Point out each Plasmodium parasite.
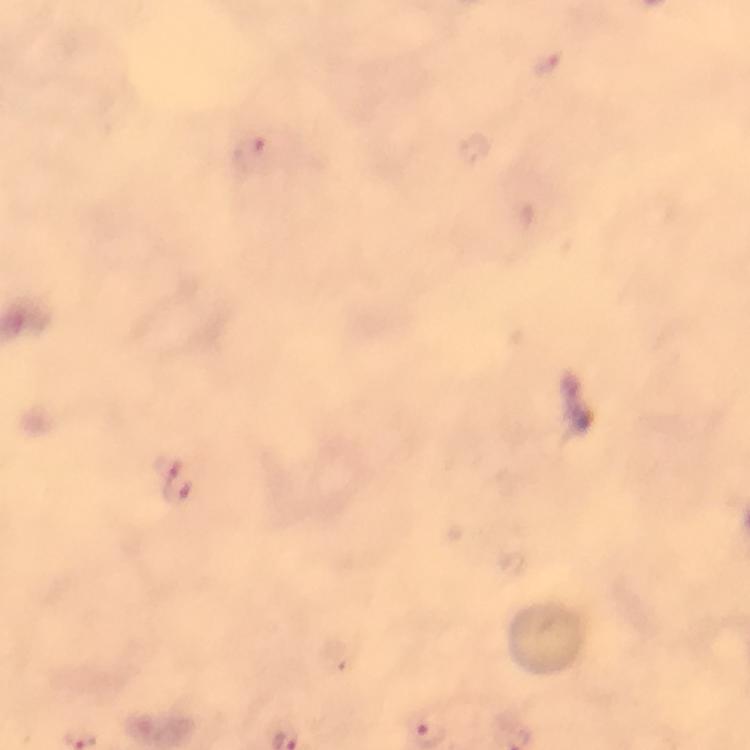
Approximate centers as {x, y} in pixels.
Plasmodium parasites: {177, 481}.

Summary:
  - Capture: smartphone photograph through a microscope
  - Image size: 750×750 pixels
  - Magnification: 100x
  - Cropped from: one field of view
  - Context: from a diagnostic examination for malaria
  - Preparation: thick blood smear
  - Immersion oil: applied
  - Stain: Giemsa